Classify this cell by malaria status.
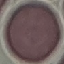

It is uninfected.

Summary:
  - Stain: Giemsa
  - Capture: smartphone camera at the microscope eyepiece
  - Image type: cell patch, automatically extracted from a larger field of view and resized to 64 × 64 pixels
  - Preparation: thin blood smear